Outline each blood parasite and name the species.
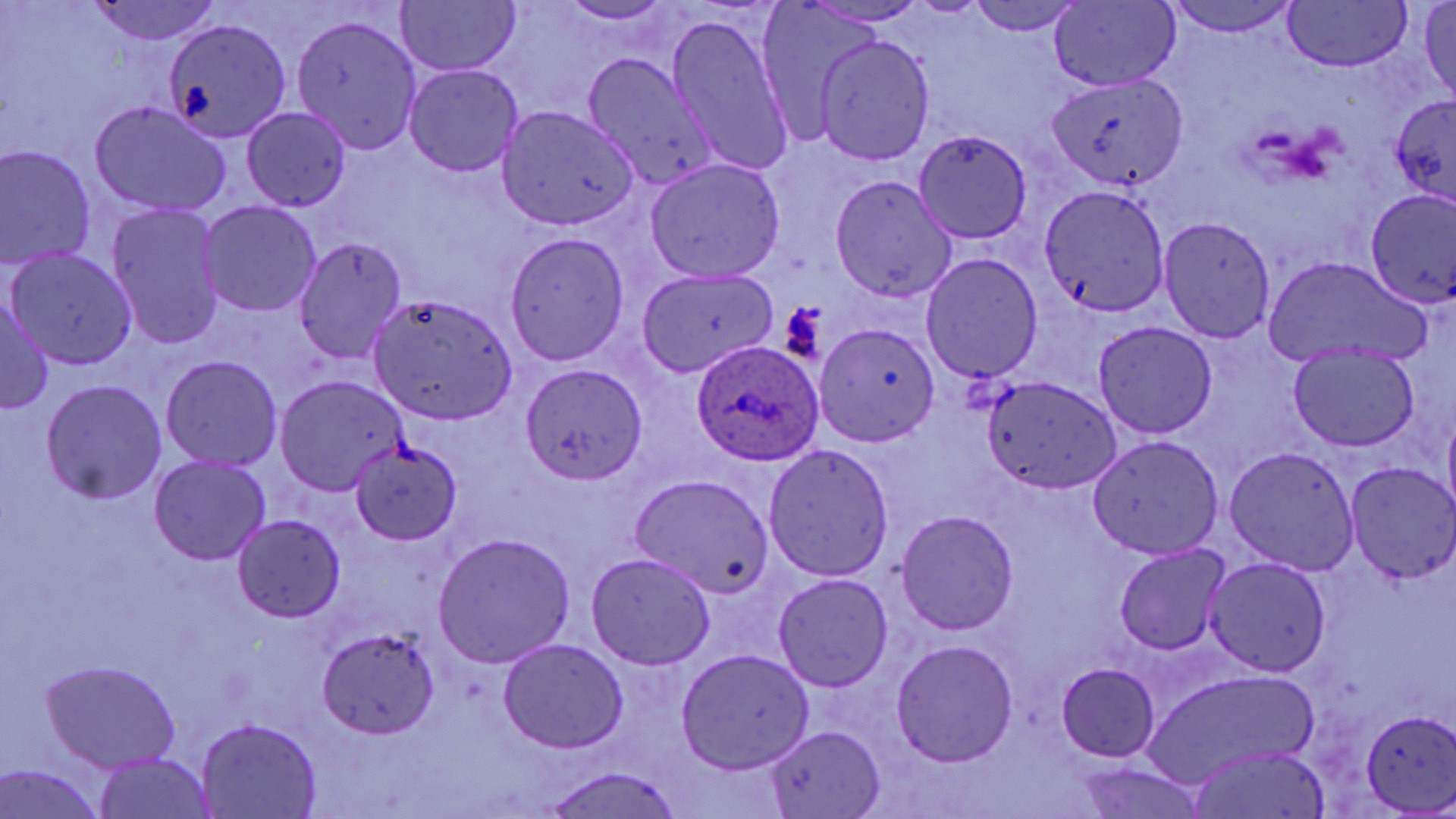

Approximate bounding boxes as (x1, y1, x2, y2) in pixels.
Plasmodium ovale-infected red blood cells: (690, 338, 824, 469).
No Plasmodium falciparum, Plasmodium malariae, Plasmodium vivax, Babesia divergens, or Trypanosoma brucei observed.

Uninfected red blood cell locations: (87, 0, 228, 49), (750, 0, 890, 149), (964, 0, 1090, 38), (1161, 0, 1301, 39), (397, 1, 519, 78), (1050, 1, 1182, 91), (556, 2, 679, 29), (1281, 2, 1412, 72), (1415, 2, 1456, 102), (663, 9, 799, 179), (289, 14, 427, 156), (161, 16, 292, 145), (807, 29, 938, 170), (580, 51, 718, 188), (1048, 54, 1188, 198), (401, 64, 523, 177), (1388, 94, 1456, 212), (86, 98, 232, 218), (497, 103, 643, 231), (239, 105, 353, 213), (911, 129, 1034, 245), (0, 142, 101, 276), (643, 157, 786, 283), (826, 175, 957, 303), (1036, 181, 1174, 322), (1363, 185, 1455, 310), (196, 200, 322, 319), (105, 202, 226, 350), (1155, 213, 1279, 346), (503, 231, 629, 366), (291, 235, 411, 363), (5, 246, 139, 371), (920, 251, 1044, 384), (1264, 255, 1433, 369), (636, 266, 777, 374), (0, 287, 53, 417), (369, 293, 517, 426), (1093, 319, 1216, 440), (816, 323, 941, 446), (1284, 341, 1423, 455), (158, 353, 285, 471), (516, 362, 647, 487), (275, 374, 408, 497), (982, 375, 1121, 496), (38, 379, 167, 504), (1085, 431, 1224, 563), (349, 438, 464, 548), (762, 444, 894, 580), (1224, 445, 1360, 576), (147, 452, 271, 565), (1344, 461, 1455, 584), (632, 474, 775, 596), (893, 507, 1021, 637), (231, 513, 347, 625), (430, 531, 576, 669), (1113, 541, 1237, 659), (585, 550, 715, 673), (1203, 553, 1330, 679), (769, 572, 895, 694), (315, 627, 443, 739), (497, 637, 628, 753), (889, 637, 1019, 768), (675, 645, 815, 776), (42, 657, 184, 772), (1051, 661, 1162, 764), (1142, 666, 1320, 788), (1356, 709, 1456, 816), (195, 717, 323, 818), (763, 725, 885, 818), (1186, 745, 1330, 819), (93, 751, 218, 819), (1068, 760, 1209, 819), (1, 761, 110, 819), (537, 768, 686, 819). Slide-level diagnosis: Plasmodium ovale. Optical microscopy. One field of a larger specimen. 1000x magnification. May-Grünwald-Giemsa stain. Thin blood smear. Image is 1456×819 pixels.